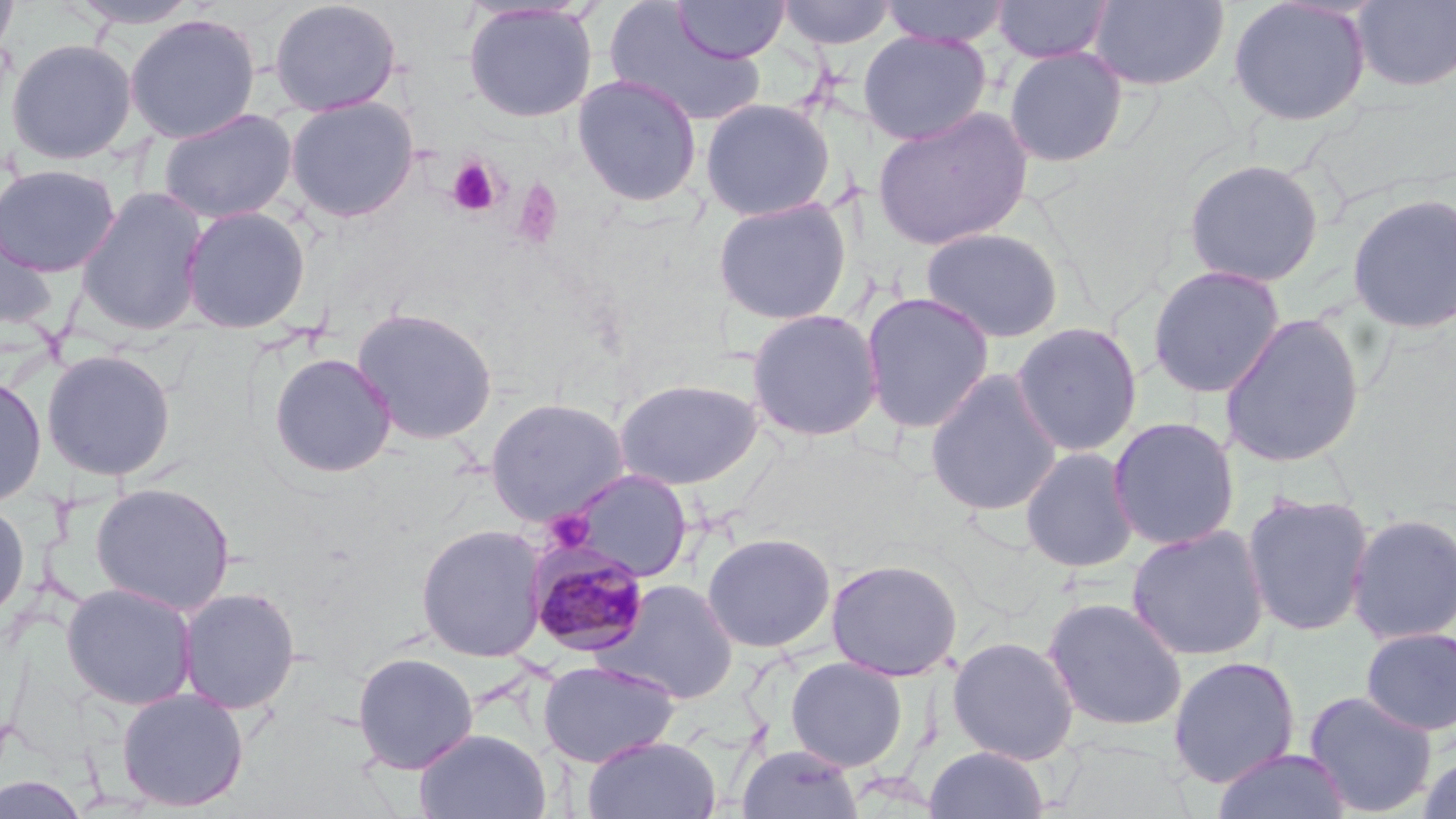 Approximate bounding boxes as named x1/y1/x2/y2 corners in pixels. Plasmodium malariae-infected red blood cell locations: (x1=528, y1=545, x2=651, y2=657). Platelet locations: (x1=445, y1=156, x2=503, y2=218), (x1=512, y1=180, x2=563, y2=250), (x1=544, y1=509, x2=594, y2=553). Uninfected red blood cell locations: (x1=0, y1=0, x2=19, y2=60), (x1=267, y1=0, x2=402, y2=117), (x1=777, y1=0, x2=897, y2=51), (x1=878, y1=0, x2=1011, y2=48), (x1=992, y1=0, x2=1114, y2=64), (x1=1088, y1=0, x2=1231, y2=91), (x1=1352, y1=0, x2=1456, y2=92), (x1=66, y1=1, x2=203, y2=29), (x1=672, y1=1, x2=790, y2=63), (x1=1227, y1=1, x2=1372, y2=126), (x1=462, y1=2, x2=598, y2=123), (x1=604, y1=3, x2=768, y2=127), (x1=125, y1=13, x2=261, y2=144), (x1=858, y1=30, x2=992, y2=144), (x1=5, y1=38, x2=138, y2=165), (x1=1003, y1=46, x2=1129, y2=167), (x1=572, y1=73, x2=703, y2=207), (x1=284, y1=95, x2=420, y2=222), (x1=699, y1=97, x2=836, y2=221), (x1=872, y1=105, x2=1033, y2=251), (x1=158, y1=108, x2=297, y2=224), (x1=1183, y1=157, x2=1325, y2=287), (x1=0, y1=163, x2=121, y2=277), (x1=75, y1=186, x2=210, y2=336), (x1=1346, y1=191, x2=1456, y2=335), (x1=712, y1=197, x2=853, y2=325), (x1=180, y1=205, x2=312, y2=333), (x1=0, y1=212, x2=59, y2=332), (x1=920, y1=226, x2=1064, y2=343), (x1=1147, y1=264, x2=1286, y2=399), (x1=860, y1=290, x2=995, y2=434), (x1=350, y1=307, x2=499, y2=445), (x1=746, y1=308, x2=884, y2=441), (x1=1218, y1=313, x2=1366, y2=469), (x1=1010, y1=321, x2=1143, y2=457), (x1=41, y1=349, x2=177, y2=481), (x1=268, y1=352, x2=398, y2=478), (x1=925, y1=369, x2=1063, y2=516), (x1=0, y1=374, x2=47, y2=508), (x1=613, y1=378, x2=763, y2=490), (x1=485, y1=397, x2=631, y2=525), (x1=1107, y1=416, x2=1241, y2=551), (x1=1019, y1=445, x2=1139, y2=573), (x1=567, y1=469, x2=693, y2=582), (x1=90, y1=481, x2=236, y2=615), (x1=1241, y1=491, x2=1375, y2=638), (x1=0, y1=498, x2=30, y2=625), (x1=1346, y1=511, x2=1456, y2=645), (x1=415, y1=524, x2=548, y2=662), (x1=1125, y1=524, x2=1270, y2=661), (x1=701, y1=532, x2=836, y2=653), (x1=826, y1=558, x2=963, y2=681), (x1=597, y1=579, x2=739, y2=704), (x1=60, y1=582, x2=198, y2=710), (x1=177, y1=586, x2=301, y2=715), (x1=1042, y1=596, x2=1188, y2=732), (x1=1359, y1=627, x2=1456, y2=737), (x1=946, y1=635, x2=1080, y2=765), (x1=351, y1=651, x2=479, y2=774), (x1=1167, y1=655, x2=1301, y2=789), (x1=785, y1=656, x2=909, y2=772), (x1=537, y1=659, x2=681, y2=767), (x1=116, y1=687, x2=250, y2=812), (x1=1303, y1=690, x2=1438, y2=817), (x1=415, y1=728, x2=552, y2=819), (x1=581, y1=735, x2=721, y2=819), (x1=736, y1=743, x2=863, y2=819), (x1=923, y1=745, x2=1049, y2=819), (x1=1211, y1=747, x2=1352, y2=819), (x1=1417, y1=752, x2=1456, y2=819), (x1=0, y1=773, x2=88, y2=818). Slide-level diagnosis: Plasmodium malariae. Thin blood smear. Captured at 1000x magnification. May-Grünwald-Giemsa-stained preparation. Single field of view. Image is 1456×819 pixels. Optical microscopy.